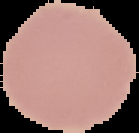 From a thin blood film. The area outside the segmented cell region is set to black. Malaria status: uninfected. Image is 139×133 pixels.